Locate every blood parasite and identify its species.
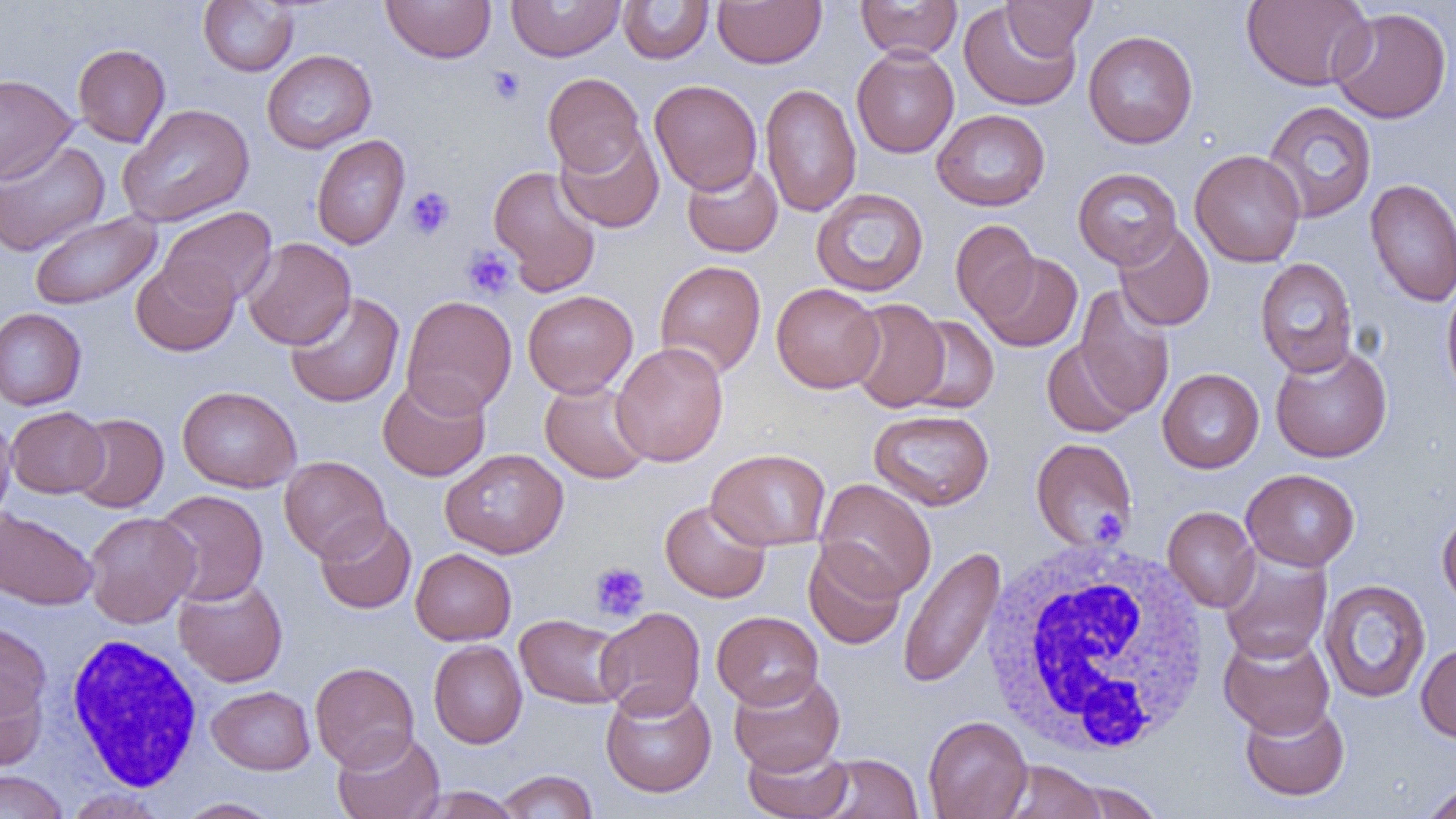

No blood parasites observed.

Summary:
  - Coordinate format: approximate bounding boxes as named x1/y1/x2/y2 corners in pixels
  - Platelet locations: (x1=488, y1=66, x2=525, y2=105), (x1=405, y1=186, x2=455, y2=239), (x1=462, y1=245, x2=517, y2=299), (x1=590, y1=562, x2=650, y2=621)
  - White blood cell locations: (x1=981, y1=538, x2=1216, y2=760), (x1=64, y1=633, x2=204, y2=791)
  - Uninfected red blood cell locations: (x1=381, y1=0, x2=497, y2=64), (x1=505, y1=0, x2=626, y2=62), (x1=712, y1=0, x2=826, y2=68), (x1=855, y1=0, x2=962, y2=61), (x1=1001, y1=0, x2=1098, y2=58), (x1=198, y1=1, x2=298, y2=76), (x1=618, y1=1, x2=713, y2=64), (x1=1241, y1=1, x2=1374, y2=91), (x1=960, y1=2, x2=1082, y2=111), (x1=1329, y1=6, x2=1452, y2=124), (x1=1083, y1=30, x2=1198, y2=149), (x1=72, y1=43, x2=171, y2=147), (x1=851, y1=45, x2=959, y2=158), (x1=262, y1=49, x2=376, y2=153), (x1=542, y1=72, x2=646, y2=177), (x1=0, y1=73, x2=77, y2=184), (x1=649, y1=79, x2=762, y2=195), (x1=760, y1=82, x2=861, y2=217), (x1=1262, y1=101, x2=1377, y2=223), (x1=117, y1=104, x2=255, y2=227), (x1=932, y1=109, x2=1050, y2=211), (x1=554, y1=126, x2=665, y2=234), (x1=312, y1=134, x2=410, y2=250), (x1=0, y1=139, x2=110, y2=256), (x1=1190, y1=149, x2=1306, y2=267), (x1=681, y1=159, x2=783, y2=258), (x1=488, y1=165, x2=602, y2=296), (x1=1072, y1=168, x2=1182, y2=270), (x1=1365, y1=178, x2=1456, y2=307), (x1=811, y1=188, x2=929, y2=297), (x1=159, y1=206, x2=278, y2=309), (x1=29, y1=211, x2=161, y2=310), (x1=950, y1=219, x2=1040, y2=321), (x1=1114, y1=222, x2=1215, y2=331), (x1=241, y1=237, x2=356, y2=350), (x1=977, y1=252, x2=1082, y2=352), (x1=131, y1=257, x2=240, y2=356), (x1=1255, y1=258, x2=1358, y2=376), (x1=654, y1=259, x2=767, y2=378), (x1=1441, y1=279, x2=1456, y2=402), (x1=771, y1=282, x2=884, y2=393), (x1=1074, y1=285, x2=1174, y2=418), (x1=522, y1=290, x2=638, y2=397), (x1=285, y1=291, x2=405, y2=408), (x1=401, y1=295, x2=517, y2=417), (x1=845, y1=299, x2=951, y2=412), (x1=0, y1=308, x2=86, y2=410), (x1=904, y1=316, x2=999, y2=413), (x1=1042, y1=339, x2=1139, y2=437), (x1=611, y1=342, x2=729, y2=466), (x1=1269, y1=343, x2=1392, y2=463), (x1=1157, y1=368, x2=1265, y2=473), (x1=378, y1=374, x2=490, y2=482), (x1=540, y1=379, x2=653, y2=484), (x1=177, y1=386, x2=302, y2=493), (x1=6, y1=406, x2=109, y2=498), (x1=869, y1=409, x2=995, y2=510), (x1=0, y1=410, x2=16, y2=523), (x1=68, y1=413, x2=168, y2=513), (x1=1030, y1=437, x2=1138, y2=552), (x1=706, y1=448, x2=831, y2=550), (x1=441, y1=449, x2=569, y2=558), (x1=279, y1=456, x2=391, y2=562), (x1=1241, y1=468, x2=1359, y2=572), (x1=816, y1=478, x2=937, y2=600), (x1=153, y1=489, x2=269, y2=605), (x1=660, y1=500, x2=771, y2=603), (x1=1163, y1=506, x2=1260, y2=612), (x1=0, y1=508, x2=99, y2=611), (x1=1437, y1=508, x2=1456, y2=614), (x1=83, y1=511, x2=199, y2=629), (x1=315, y1=514, x2=417, y2=614), (x1=803, y1=542, x2=906, y2=650), (x1=898, y1=545, x2=1006, y2=689), (x1=410, y1=548, x2=516, y2=645), (x1=1218, y1=548, x2=1333, y2=663), (x1=174, y1=577, x2=288, y2=687), (x1=1319, y1=579, x2=1431, y2=703), (x1=595, y1=607, x2=706, y2=719), (x1=711, y1=610, x2=823, y2=709), (x1=514, y1=613, x2=628, y2=709), (x1=0, y1=621, x2=52, y2=735), (x1=1218, y1=630, x2=1335, y2=739), (x1=428, y1=640, x2=527, y2=748), (x1=1416, y1=641, x2=1456, y2=743), (x1=310, y1=661, x2=419, y2=771), (x1=0, y1=667, x2=48, y2=772), (x1=728, y1=669, x2=845, y2=776), (x1=600, y1=683, x2=717, y2=798), (x1=207, y1=685, x2=315, y2=774), (x1=1240, y1=700, x2=1350, y2=801), (x1=923, y1=715, x2=1032, y2=819), (x1=331, y1=728, x2=445, y2=819), (x1=742, y1=743, x2=854, y2=818), (x1=816, y1=754, x2=924, y2=819), (x1=998, y1=760, x2=1106, y2=819), (x1=0, y1=770, x2=68, y2=819), (x1=495, y1=770, x2=598, y2=818), (x1=1062, y1=780, x2=1165, y2=818), (x1=1420, y1=780, x2=1456, y2=819), (x1=414, y1=786, x2=523, y2=818), (x1=63, y1=787, x2=170, y2=819), (x1=174, y1=797, x2=284, y2=818)
  - Slide-level diagnosis: negative for blood parasites
  - Magnification: 1000x
  - Modality: light microscopy
  - Preparation: thin blood film
  - Field of view: one of a larger specimen
  - Image size: 1456×819 pixels